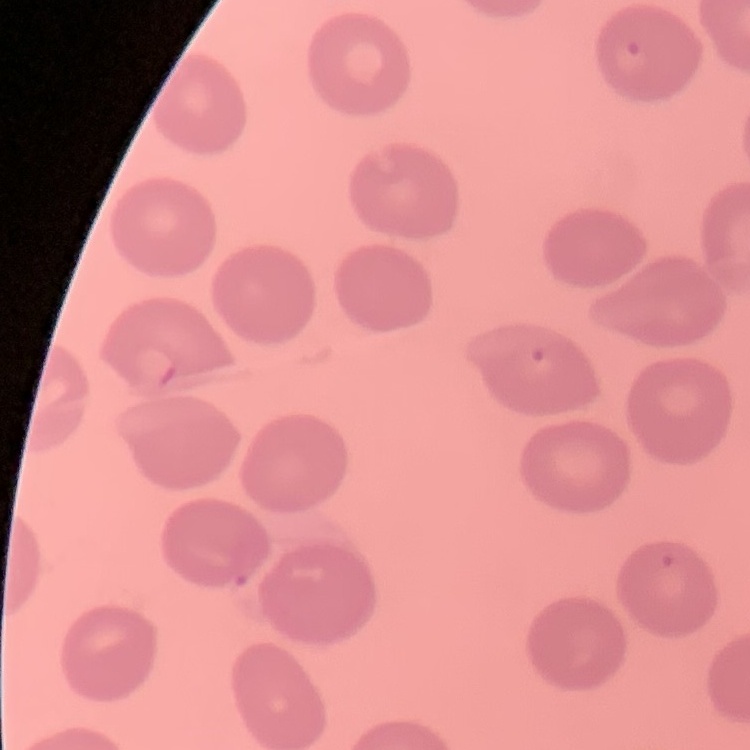
Summary:
  - Red blood cell morphology: no rouleaux formation
  - Stain: Field's or Giemsa
  - Image type: one tile cut from a larger photomicrograph
  - Preparation: thin blood smear